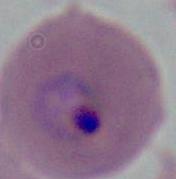
Summary:
  - Modality: micrograph
  - Magnification: 400x or 1000x
  - Identification: Plasmodium